Comment on the morphology of the red blood cells.
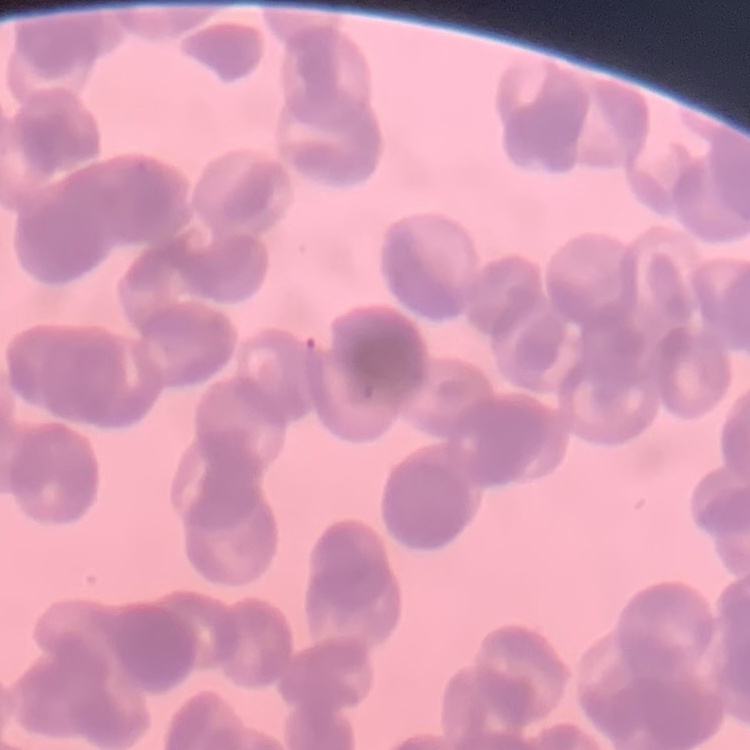

They show rouleaux formation.

image type = one tile cut from a larger photomicrograph
preparation = thin blood film
stain = Field's or Giemsa